Report the malaria status of this cell.
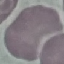

It is uninfected.

stain: Giemsa
preparation: thin smear
image_type: cell patch, automatically extracted from a larger field of view and resized to 64 × 64 pixels
capture: smartphone camera at the microscope eyepiece